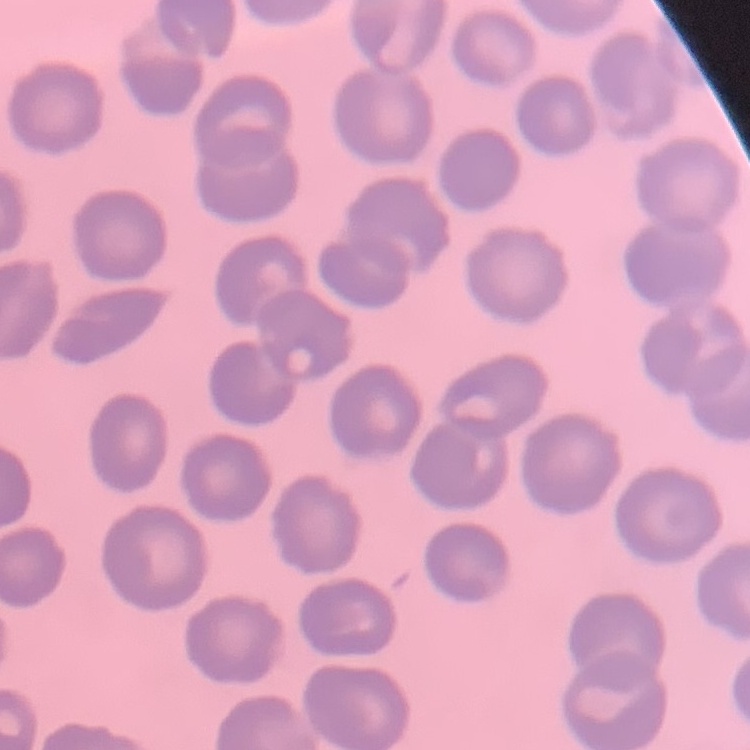 The erythrocytes show no rouleaux formation. Square crop of a larger photomicrograph. Thin blood smear. Field's or Giemsa stain.